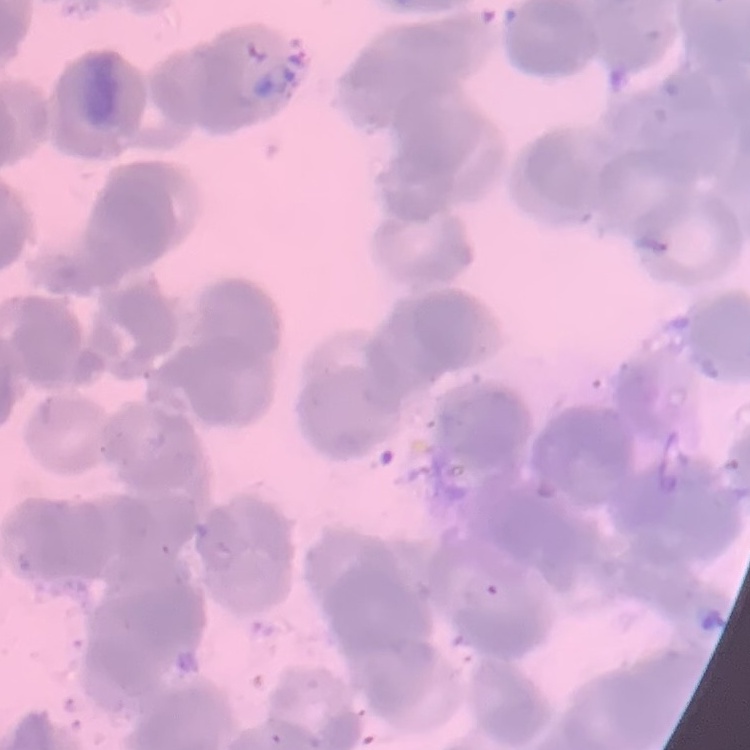
Summary:
  - Erythrocyte morphology: rouleaux formation
  - Preparation: thin peripheral smear
  - Stain: Field's or Giemsa
  - Image type: square crop of a larger photomicrograph